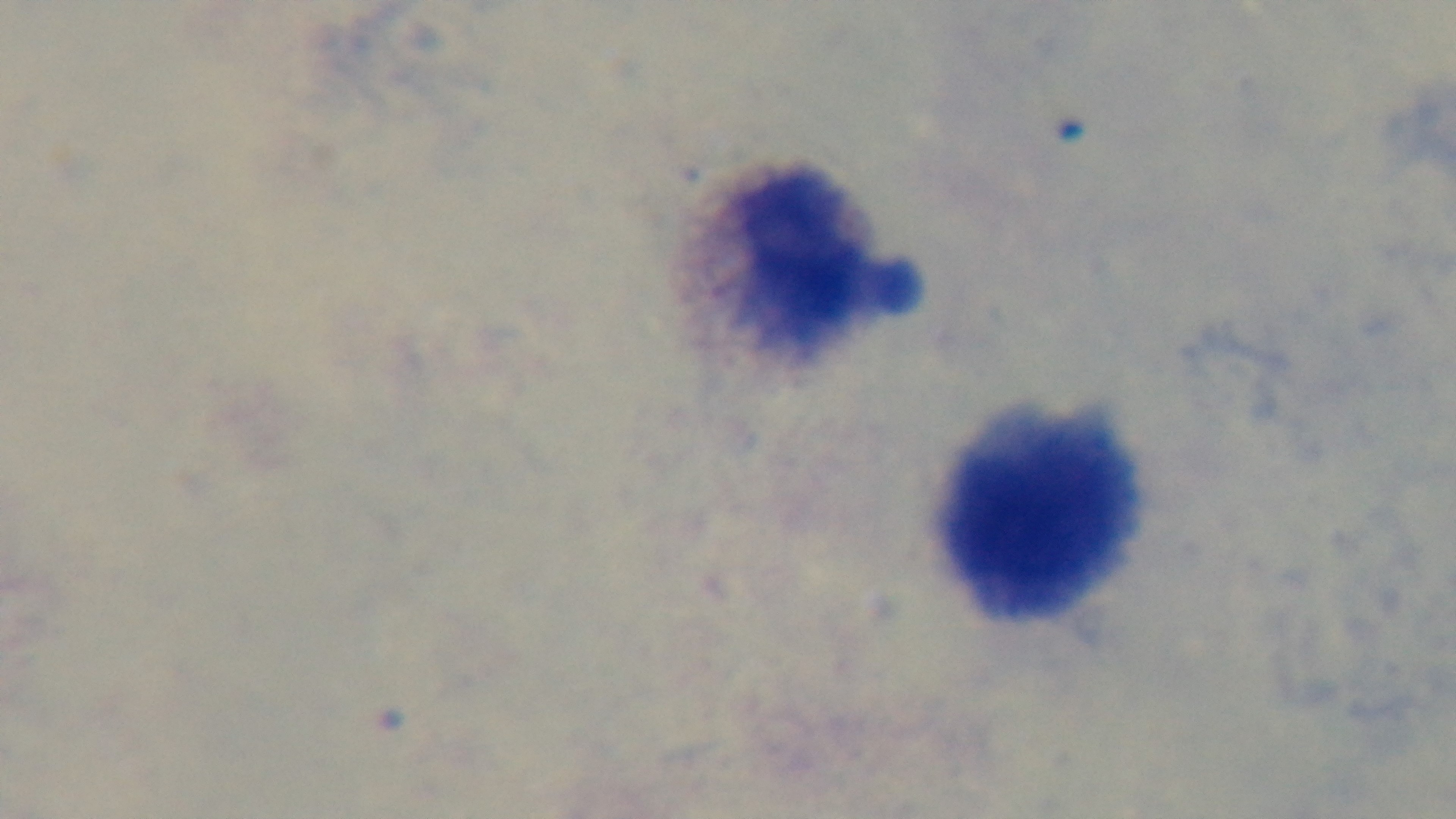 Giemsa-stained. Malaria status: uninfected. Oil-immersion objective, 100x. Preparation: thick blood film. Photomicrograph. Mounted 4K digital camera. Single field of view.